Outline each Plasmodium malariae-infected red blood cell.
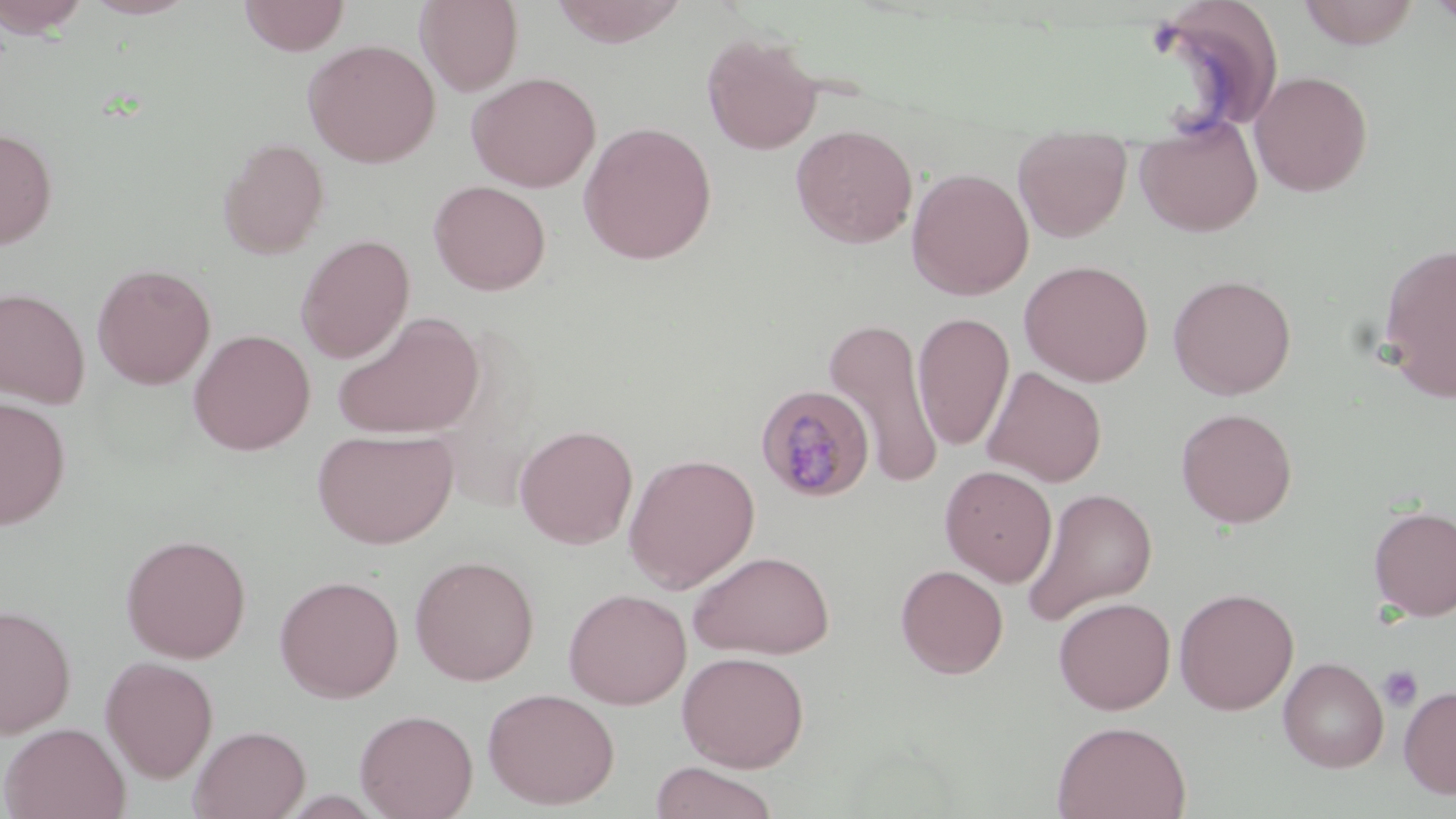
Approximate bounding boxes as (x1, y1, x2, y2) in pixels.
Plasmodium malariae-infected red blood cells: (755, 384, 876, 503).

Platelet locations: (1378, 665, 1423, 713). Uninfected red blood cell locations: (0, 0, 93, 38), (79, 0, 201, 19), (238, 0, 350, 55), (415, 0, 523, 96), (550, 0, 689, 47), (1296, 0, 1422, 49), (1426, 0, 1456, 31), (701, 32, 823, 154), (302, 38, 441, 168), (1249, 70, 1374, 197), (466, 71, 601, 193), (1134, 115, 1263, 237), (578, 120, 717, 264), (790, 124, 918, 248), (0, 126, 58, 250), (1013, 135, 1132, 242), (217, 137, 330, 259), (906, 167, 1034, 300), (428, 180, 551, 296), (296, 234, 415, 364), (1376, 242, 1456, 401), (1019, 259, 1155, 387), (92, 262, 216, 390), (1168, 273, 1297, 400), (0, 286, 91, 409), (332, 310, 484, 440), (913, 311, 1014, 452), (824, 316, 943, 490), (188, 329, 315, 455), (982, 366, 1106, 487), (0, 395, 71, 530), (1176, 407, 1298, 528), (515, 424, 638, 549), (313, 428, 457, 548), (623, 452, 760, 593), (939, 464, 1057, 586), (1022, 486, 1158, 625), (1368, 504, 1456, 621), (120, 533, 251, 662), (687, 550, 836, 660), (409, 554, 540, 686), (895, 564, 1008, 678), (274, 573, 404, 703), (1174, 587, 1298, 715), (563, 588, 692, 709), (1053, 596, 1176, 715), (0, 603, 77, 738), (676, 650, 809, 771), (100, 655, 219, 783), (1278, 656, 1389, 772), (1398, 685, 1456, 799), (482, 687, 620, 810), (354, 708, 478, 819), (1052, 719, 1192, 819), (1, 722, 130, 819), (188, 725, 311, 819), (649, 762, 780, 819). Slide-level diagnosis: Plasmodium malariae. Thin blood film. One field of a larger specimen. Image is 1456×819 pixels. 1000x magnification. Optical microscopy. May-Grünwald-Giemsa stain.